Locate every uninfected red blood cell.
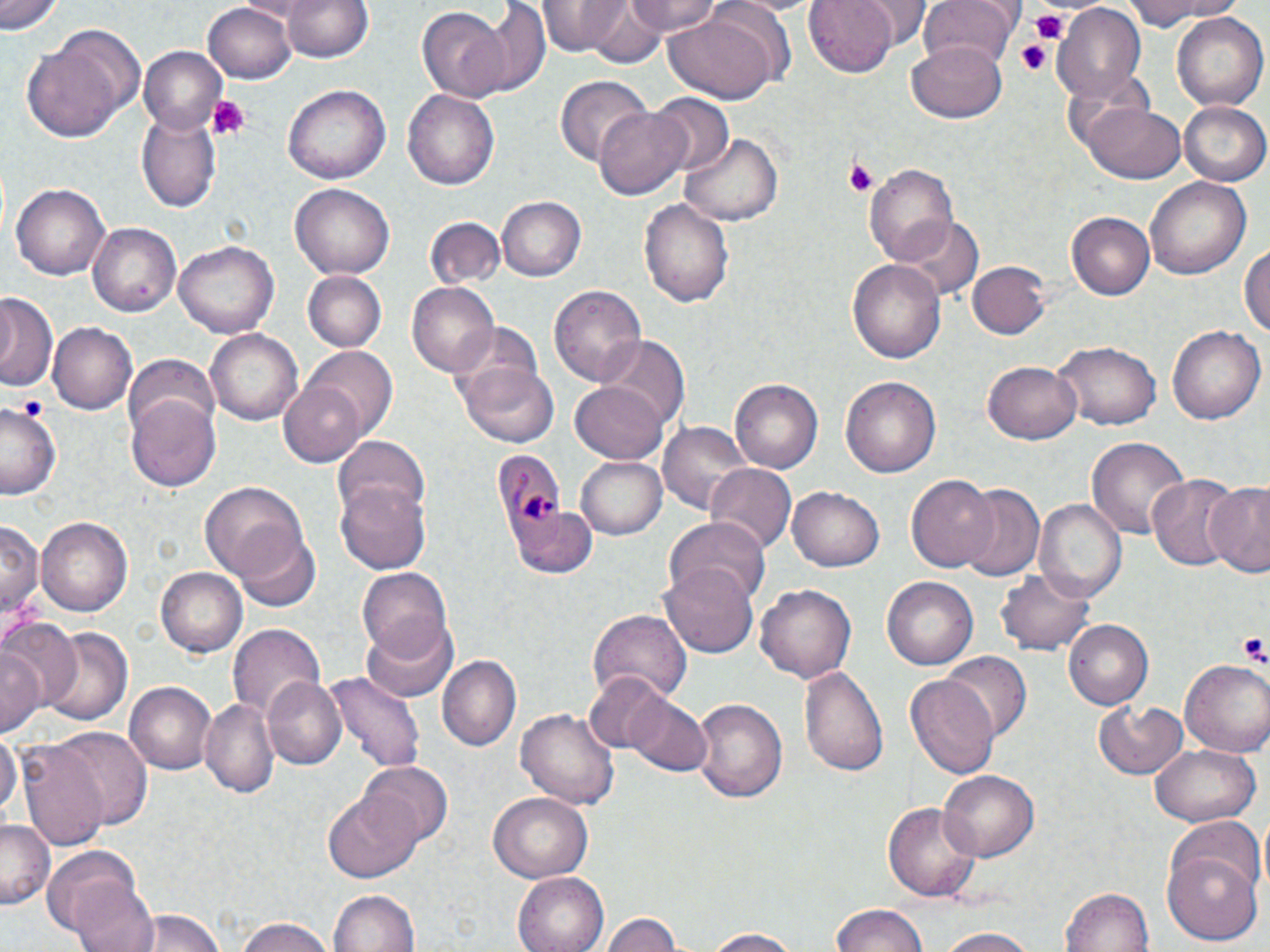
Approximate bounding boxes as [x1, y1, x2, y2] in pixels.
Uninfected red blood cells: [2, 0, 62, 36], [280, 0, 377, 64], [538, 0, 641, 58], [620, 0, 728, 41], [721, 0, 826, 18], [804, 0, 899, 76], [856, 0, 930, 44], [916, 0, 1017, 72], [1117, 0, 1250, 26], [472, 1, 551, 96], [202, 3, 296, 84], [582, 3, 670, 70], [1054, 5, 1148, 102], [418, 6, 509, 101], [663, 11, 779, 104], [1171, 11, 1268, 112], [21, 40, 129, 146], [906, 43, 1011, 124], [137, 46, 229, 133], [554, 75, 649, 167], [285, 85, 390, 184], [403, 88, 499, 192], [647, 94, 733, 177], [1082, 102, 1185, 183], [1179, 102, 1270, 188], [592, 104, 692, 202], [137, 109, 221, 212], [682, 134, 784, 226], [866, 163, 959, 268], [1145, 176, 1251, 279], [10, 182, 111, 281], [291, 185, 394, 279], [497, 196, 586, 280], [640, 198, 735, 307], [1064, 210, 1155, 300], [899, 217, 983, 304], [423, 218, 505, 290], [86, 220, 181, 313], [1241, 235, 1270, 345], [175, 239, 279, 336], [848, 259, 945, 367], [967, 259, 1050, 339], [303, 270, 384, 351], [549, 282, 648, 386], [406, 283, 499, 380], [0, 294, 55, 393], [47, 322, 138, 415], [1167, 324, 1263, 425], [204, 328, 305, 426], [598, 339, 688, 434], [1055, 339, 1161, 431], [303, 346, 400, 439], [122, 352, 220, 436], [984, 357, 1082, 444], [454, 360, 559, 448], [840, 375, 942, 479], [730, 378, 822, 473], [279, 380, 367, 465], [571, 382, 671, 464], [129, 399, 221, 491], [1, 401, 62, 498], [660, 421, 754, 519], [332, 433, 431, 525], [1086, 436, 1190, 544], [576, 455, 666, 540], [706, 465, 795, 556], [905, 473, 1000, 574], [1146, 475, 1239, 569], [200, 479, 307, 582], [337, 480, 431, 575], [1201, 482, 1270, 576], [953, 484, 1046, 582], [788, 485, 885, 572], [1037, 497, 1127, 601], [510, 507, 597, 579], [37, 515, 132, 618], [665, 516, 771, 606], [1, 518, 41, 621], [231, 526, 322, 612], [661, 561, 758, 659], [998, 566, 1099, 656], [155, 567, 246, 656], [358, 569, 451, 661], [882, 576, 979, 671], [757, 583, 857, 684], [588, 608, 691, 704], [0, 618, 81, 711], [359, 619, 459, 703], [1063, 620, 1152, 710], [229, 622, 327, 718], [35, 623, 133, 730], [1, 639, 43, 739], [941, 650, 1030, 741], [439, 656, 521, 751], [1179, 659, 1270, 755], [801, 665, 889, 779], [322, 671, 426, 773], [585, 674, 672, 753], [905, 674, 1001, 781], [263, 676, 347, 771], [123, 682, 215, 775], [624, 691, 710, 776], [199, 697, 279, 796], [691, 698, 786, 803], [1091, 698, 1190, 779], [514, 708, 621, 811], [0, 727, 19, 822], [52, 728, 151, 828], [20, 740, 109, 850], [1148, 744, 1261, 828], [359, 762, 453, 850], [938, 770, 1040, 861], [324, 787, 422, 882], [487, 792, 594, 882], [884, 799, 982, 904], [1166, 814, 1263, 898], [0, 818, 52, 906], [42, 844, 147, 939], [1163, 848, 1262, 945], [514, 872, 608, 952], [68, 878, 162, 952], [1061, 886, 1155, 952], [325, 889, 422, 952], [830, 905, 928, 952], [123, 910, 230, 952], [599, 911, 687, 952], [231, 916, 339, 952], [934, 927, 1045, 952], [698, 928, 809, 951].

slide-level diagnosis = Plasmodium malariae
platelet locations = approximate bounding boxes as [x1, y1, x2, y2] in pixels: [1030, 12, 1067, 42], [1018, 41, 1050, 77], [207, 95, 253, 143], [843, 158, 880, 196], [17, 393, 47, 419], [1239, 632, 1268, 666]
field of view = one of a larger specimen
stain = May-Grünwald-Giemsa
preparation = thin blood film
magnification = 1000x
image size = 1270×952 pixels
modality = optical microscopy
Plasmodium malariae-infected red blood cell locations = approximate bounding boxes as [x1, y1, x2, y2] in pixels: [493, 452, 565, 541]